Outline each uninfected red blood cell.
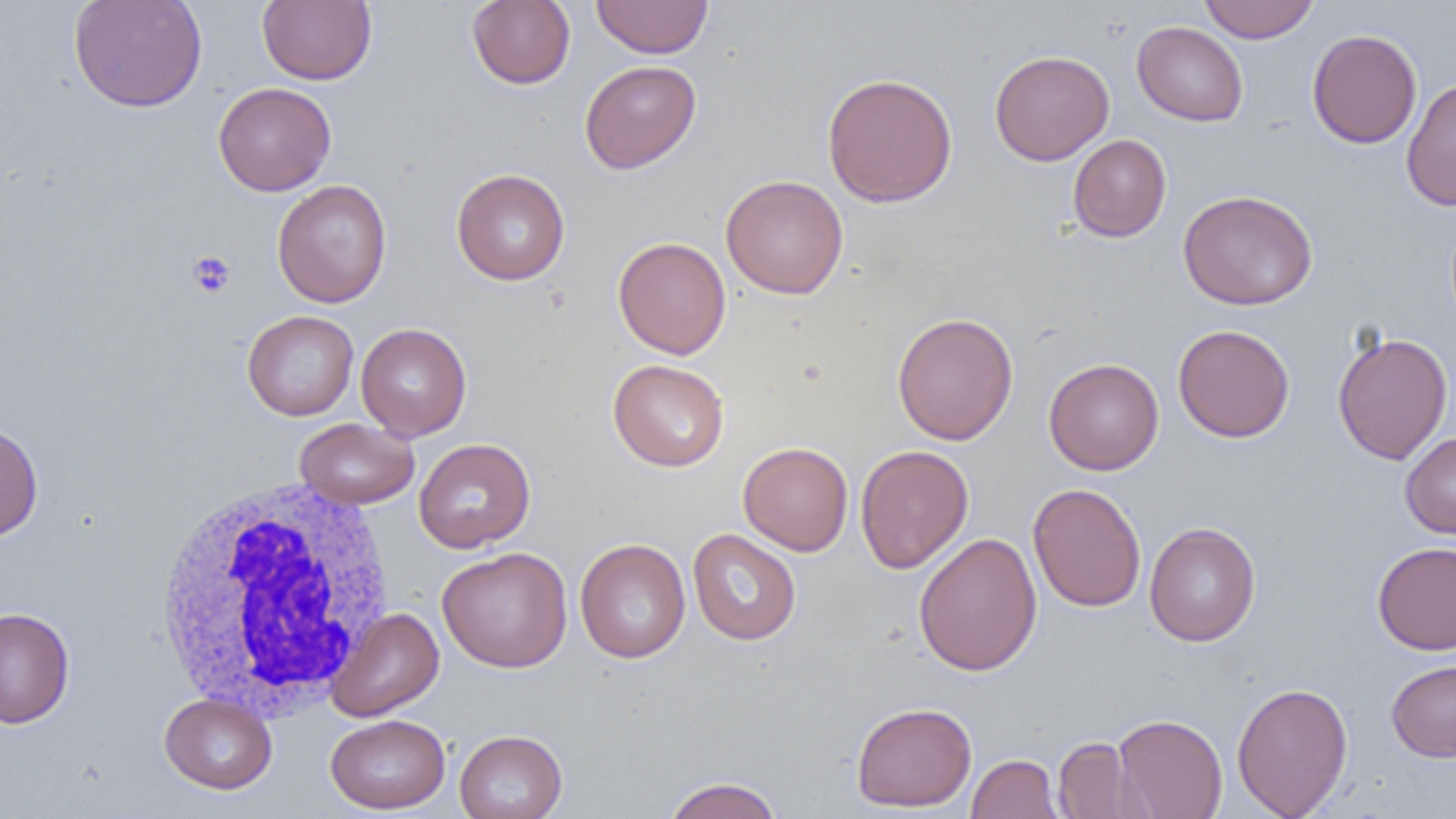
Approximate bounding boxes as (x1,y1)-(x2,y2) corner pairs in pixels.
Uninfected red blood cells: (68,0)-(207,113), (257,0)-(377,85), (466,0)-(576,90), (591,0)-(713,58), (1199,0)-(1320,43), (1132,21)-(1249,126), (1306,28)-(1422,149), (989,49)-(1114,166), (579,60)-(701,174), (822,72)-(958,208), (1401,78)-(1456,212), (213,82)-(336,196), (1067,134)-(1171,242), (451,168)-(570,285), (721,174)-(849,300), (272,179)-(392,308), (1178,189)-(1318,310), (613,236)-(731,359), (242,310)-(359,420), (892,312)-(1019,445), (355,322)-(472,441), (1172,324)-(1295,442), (1331,330)-(1453,465), (1043,357)-(1164,476), (608,358)-(730,472), (295,417)-(419,509), (0,422)-(43,542), (1400,432)-(1456,540), (414,437)-(536,553), (738,442)-(854,555), (855,444)-(973,574), (1028,483)-(1146,612), (1144,521)-(1261,647), (687,529)-(801,646), (913,532)-(1043,676), (574,537)-(690,664), (1372,541)-(1456,655), (437,546)-(573,673), (0,607)-(75,728), (326,607)-(444,722), (1385,659)-(1456,762), (1231,681)-(1353,818), (159,692)-(277,794), (850,701)-(977,812), (1113,713)-(1228,819), (325,714)-(451,814), (454,729)-(568,819), (1053,736)-(1149,818), (967,753)-(1063,818), (661,775)-(785,819).

Summary:
  - White blood cell locations: (151,477)-(396,721)
  - Platelet locations: (187,251)-(236,298)
  - Slide-level diagnosis: negative for blood parasites
  - Field of view: single
  - Preparation: thin blood smear
  - Magnification: 1000x
  - Image size: 1456×819 pixels
  - Modality: optical microscopy